Identify the blood parasite species.
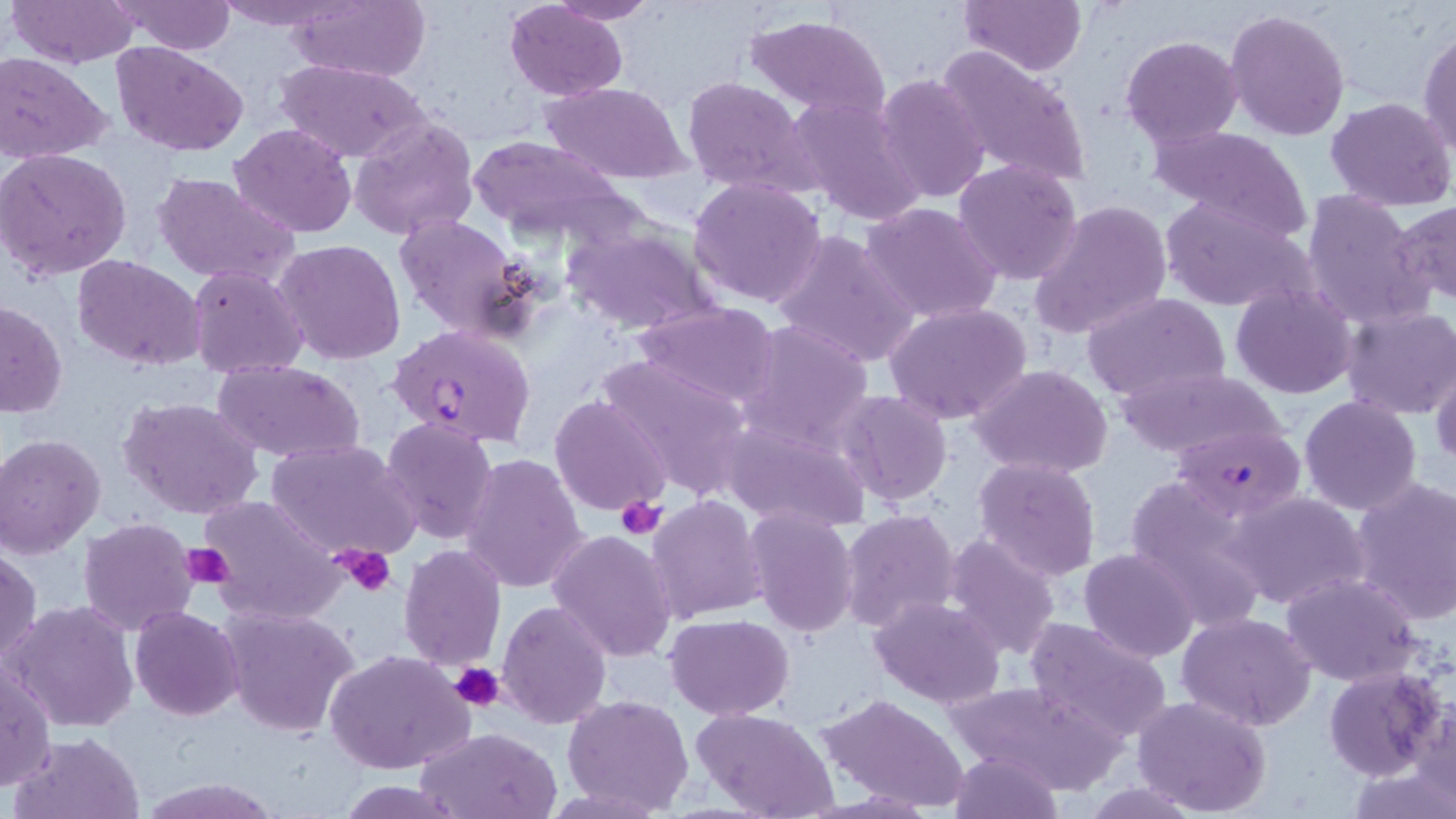
Plasmodium falciparum.

Approximate bounding boxes as (x1, y1, x2, y2) in pixels. Uninfected red blood cell locations: (7, 0, 139, 69), (213, 0, 346, 30), (281, 0, 432, 84), (961, 0, 1088, 75), (109, 1, 238, 55), (544, 1, 661, 24), (504, 2, 629, 100), (1224, 7, 1351, 142), (744, 12, 891, 122), (1418, 26, 1456, 155), (1120, 35, 1244, 150), (111, 43, 250, 158), (936, 43, 1092, 191), (0, 51, 114, 164), (277, 59, 427, 165), (876, 73, 990, 205), (680, 75, 821, 201), (542, 82, 690, 184), (788, 95, 926, 226), (1326, 96, 1456, 209), (348, 115, 478, 241), (231, 123, 358, 238), (1151, 125, 1313, 241), (464, 135, 634, 244), (0, 149, 132, 279), (953, 158, 1084, 285), (151, 171, 300, 287), (687, 176, 827, 308), (1301, 190, 1433, 330), (1159, 197, 1310, 312), (1395, 198, 1456, 307), (1029, 200, 1173, 341), (861, 202, 1004, 325), (391, 212, 532, 341), (561, 222, 719, 335), (772, 228, 919, 369), (273, 239, 407, 366), (71, 254, 207, 371), (189, 265, 309, 380), (1230, 282, 1358, 398), (1081, 291, 1230, 405), (0, 301, 68, 418), (635, 301, 782, 409), (886, 303, 1032, 426), (1340, 306, 1455, 420), (737, 318, 875, 451), (592, 353, 753, 500), (1429, 357, 1455, 472), (211, 359, 366, 463), (969, 365, 1113, 479), (1114, 367, 1287, 459), (836, 390, 953, 505), (118, 395, 264, 521), (551, 395, 672, 516), (1299, 395, 1422, 515), (379, 415, 499, 545), (716, 416, 870, 532), (0, 432, 108, 559), (267, 440, 421, 562), (462, 453, 589, 594), (972, 455, 1101, 581), (1124, 475, 1273, 633), (1349, 475, 1456, 625), (1227, 490, 1371, 610), (197, 493, 346, 624), (647, 495, 768, 622), (743, 508, 860, 637), (840, 508, 962, 632), (78, 517, 200, 637), (547, 529, 677, 664), (942, 533, 1063, 662), (1, 543, 42, 666), (397, 544, 507, 672), (1079, 548, 1199, 661), (1277, 573, 1426, 687), (868, 595, 1006, 708), (497, 599, 612, 730), (4, 601, 141, 731), (219, 605, 360, 739), (130, 606, 244, 720), (1177, 612, 1317, 731), (666, 613, 794, 720), (1023, 618, 1174, 743), (326, 649, 474, 776), (0, 659, 55, 791), (1322, 666, 1447, 780), (945, 678, 1125, 792), (818, 692, 970, 812), (561, 693, 694, 813), (1132, 695, 1271, 817), (1409, 702, 1455, 816), (693, 707, 839, 819), (414, 727, 561, 818), (10, 731, 146, 819), (949, 749, 1062, 819), (136, 774, 280, 817), (1078, 781, 1208, 817). Plasmodium falciparum-infected red blood cell locations: (388, 322, 537, 449), (1170, 424, 1305, 520). Platelet locations: (614, 495, 667, 540), (182, 543, 235, 589), (336, 546, 397, 596), (449, 662, 505, 713). Thin blood smear. Captured at 1000x magnification. Image is 1456×819 pixels. Single field of view. May-Grünwald-Giemsa-stained preparation. Optical microscopy.